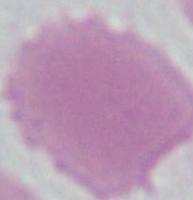

magnification = 1000x
modality = micrograph
identification = red blood cell